State which parasite is depicted.
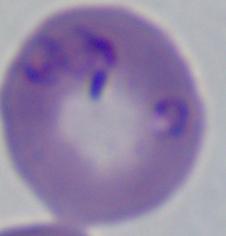
This is Babesia.

{
  "magnification": "1000x",
  "modality": "photomicrograph"
}